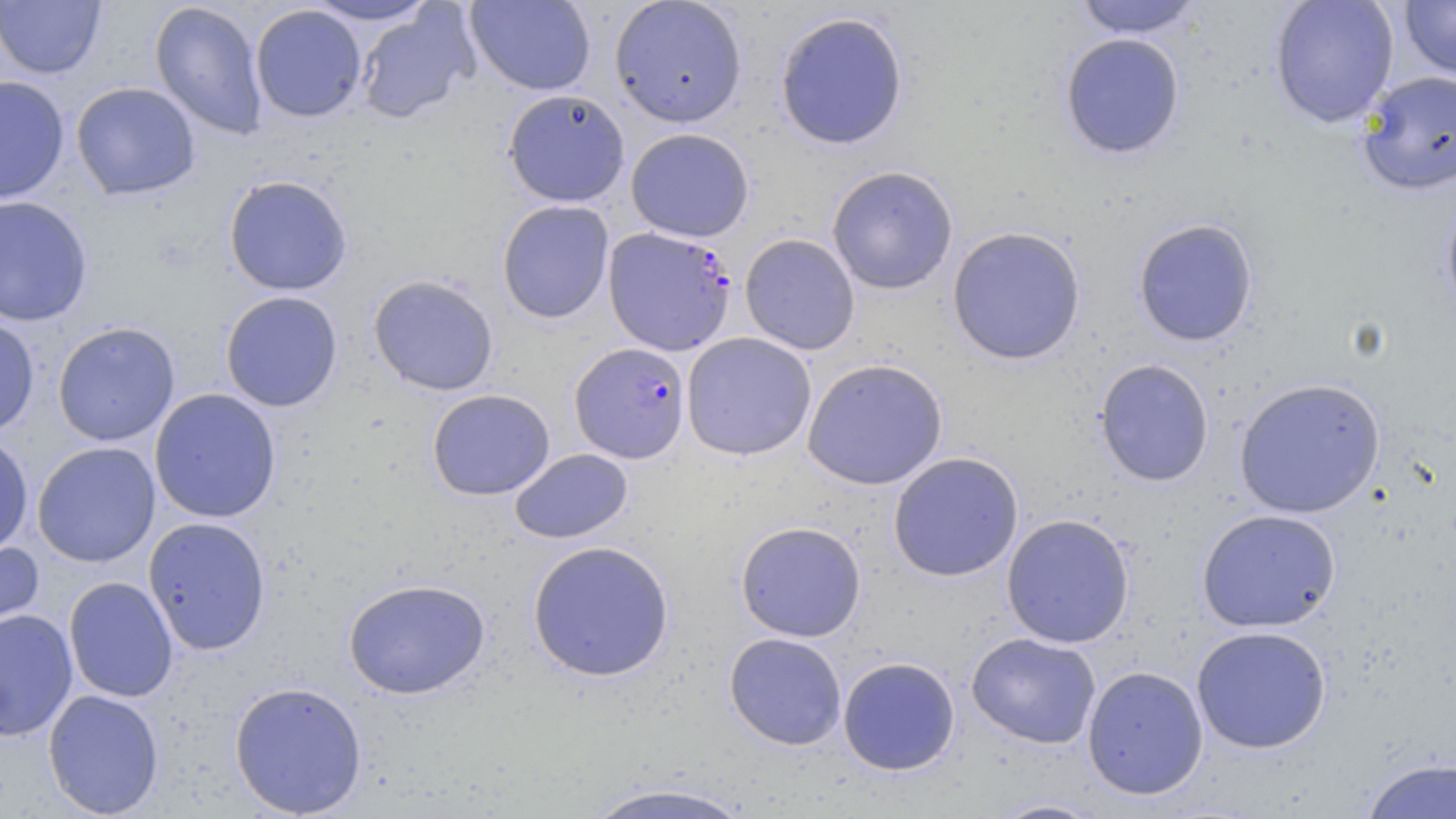
Summary:
  - Coordinate format: approximate bounding boxes as named x1/y1/x2/y2 corners in pixels
  - Uninfected red blood cell locations: (x1=304, y1=0, x2=436, y2=26), (x1=465, y1=0, x2=596, y2=95), (x1=609, y1=0, x2=748, y2=128), (x1=1072, y1=0, x2=1203, y2=38), (x1=1269, y1=0, x2=1399, y2=128), (x1=1399, y1=0, x2=1456, y2=80), (x1=0, y1=1, x2=106, y2=79), (x1=149, y1=1, x2=268, y2=140), (x1=250, y1=4, x2=367, y2=122), (x1=355, y1=4, x2=480, y2=125), (x1=774, y1=10, x2=910, y2=151), (x1=1060, y1=32, x2=1185, y2=159), (x1=1357, y1=70, x2=1456, y2=195), (x1=0, y1=75, x2=70, y2=204), (x1=70, y1=82, x2=201, y2=201), (x1=502, y1=89, x2=630, y2=207), (x1=625, y1=127, x2=755, y2=242), (x1=826, y1=165, x2=958, y2=295), (x1=223, y1=174, x2=353, y2=296), (x1=1440, y1=188, x2=1456, y2=325), (x1=0, y1=194, x2=94, y2=327), (x1=496, y1=199, x2=615, y2=324), (x1=1132, y1=218, x2=1259, y2=347), (x1=947, y1=226, x2=1086, y2=365), (x1=739, y1=233, x2=861, y2=355), (x1=367, y1=274, x2=499, y2=396), (x1=220, y1=291, x2=343, y2=412), (x1=0, y1=315, x2=40, y2=437), (x1=52, y1=321, x2=180, y2=446), (x1=681, y1=332, x2=817, y2=461), (x1=801, y1=358, x2=949, y2=491), (x1=1094, y1=358, x2=1215, y2=487), (x1=1234, y1=377, x2=1385, y2=518), (x1=149, y1=388, x2=282, y2=523), (x1=427, y1=388, x2=555, y2=501), (x1=0, y1=430, x2=34, y2=558), (x1=32, y1=441, x2=161, y2=567), (x1=509, y1=448, x2=633, y2=544), (x1=887, y1=451, x2=1024, y2=582), (x1=1196, y1=508, x2=1341, y2=633), (x1=1001, y1=513, x2=1136, y2=648), (x1=143, y1=516, x2=272, y2=655), (x1=735, y1=520, x2=867, y2=642), (x1=0, y1=535, x2=44, y2=648), (x1=526, y1=540, x2=675, y2=683), (x1=64, y1=576, x2=179, y2=703), (x1=343, y1=577, x2=491, y2=699), (x1=0, y1=608, x2=78, y2=741), (x1=1191, y1=625, x2=1331, y2=754), (x1=723, y1=632, x2=847, y2=750), (x1=966, y1=632, x2=1102, y2=749), (x1=838, y1=656, x2=961, y2=776), (x1=1082, y1=665, x2=1208, y2=800), (x1=228, y1=680, x2=368, y2=818), (x1=42, y1=688, x2=165, y2=818), (x1=1359, y1=756, x2=1456, y2=818), (x1=578, y1=780, x2=758, y2=819), (x1=986, y1=797, x2=1112, y2=818)
  - Plasmodium falciparum-infected red blood cell locations: (x1=603, y1=226, x2=738, y2=356), (x1=569, y1=342, x2=691, y2=463)
  - Slide-level diagnosis: Plasmodium falciparum
  - Preparation: thin blood smear
  - Stain: May-Grünwald-Giemsa
  - Image size: 1456×819 pixels
  - Magnification: 1000x
  - Field of view: single
  - Modality: optical microscopy